Locate and identify every blood parasite.
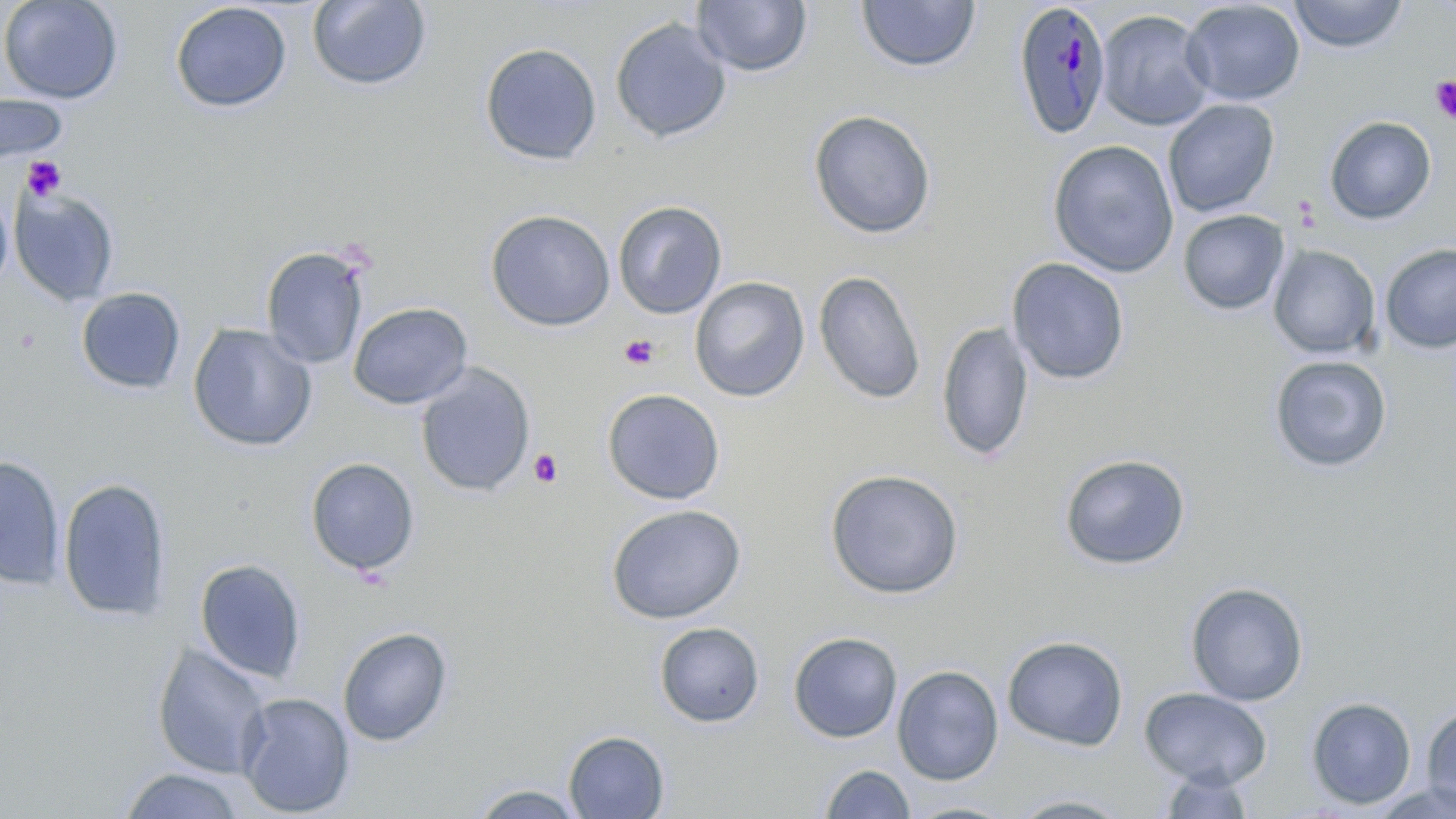

Approximate bounding boxes as [x1, y1, x2, y2] in pixels.
Plasmodium malariae-infected red blood cells: [1011, 1, 1112, 140].
No Plasmodium falciparum, Plasmodium ovale, Plasmodium vivax, Babesia divergens, or Trypanosoma brucei observed.

Summary:
  - Uninfected red blood cell locations: [0, 0, 123, 104], [307, 0, 432, 91], [856, 0, 981, 74], [1288, 0, 1409, 53], [693, 1, 812, 78], [1180, 1, 1306, 106], [169, 2, 292, 114], [1096, 9, 1215, 131], [610, 17, 732, 144], [479, 42, 603, 165], [1, 92, 69, 164], [1163, 99, 1280, 217], [808, 109, 936, 240], [1324, 116, 1437, 224], [1048, 139, 1179, 277], [0, 185, 14, 295], [9, 187, 120, 307], [613, 200, 727, 319], [485, 209, 616, 332], [1177, 209, 1289, 315], [1380, 243, 1456, 353], [1268, 245, 1381, 359], [261, 246, 370, 370], [1006, 257, 1130, 385], [813, 269, 926, 405], [689, 276, 810, 402], [76, 287, 186, 395], [348, 301, 473, 409], [936, 321, 1035, 464], [186, 323, 318, 452], [1268, 355, 1392, 473], [415, 364, 536, 497], [602, 388, 725, 505], [1059, 453, 1191, 570], [0, 455, 65, 590], [305, 457, 421, 577], [824, 468, 964, 600], [57, 477, 172, 622], [605, 504, 747, 625], [194, 558, 307, 682], [1185, 582, 1308, 706], [654, 621, 765, 728], [338, 626, 453, 746], [788, 631, 903, 743], [1002, 635, 1128, 751], [151, 641, 274, 780], [892, 664, 1004, 785], [1140, 687, 1272, 789], [236, 692, 355, 817], [1306, 696, 1417, 810], [1421, 704, 1456, 814], [563, 730, 670, 819], [819, 763, 915, 819], [1155, 767, 1257, 818], [119, 768, 246, 818], [1368, 780, 1456, 819], [467, 784, 588, 818], [1006, 792, 1134, 818], [902, 801, 1019, 818]
  - Platelet locations: [1430, 75, 1456, 124], [21, 156, 67, 201], [10, 324, 42, 357], [619, 335, 659, 369], [528, 448, 563, 488]
  - Slide-level diagnosis: Plasmodium malariae
  - Field of view: one of a larger specimen
  - Magnification: 1000x
  - Modality: light microscopy
  - Stain: May-Grünwald-Giemsa
  - Image size: 1456×819 pixels
  - Preparation: thin blood film